Look for Plasmodium parasites.
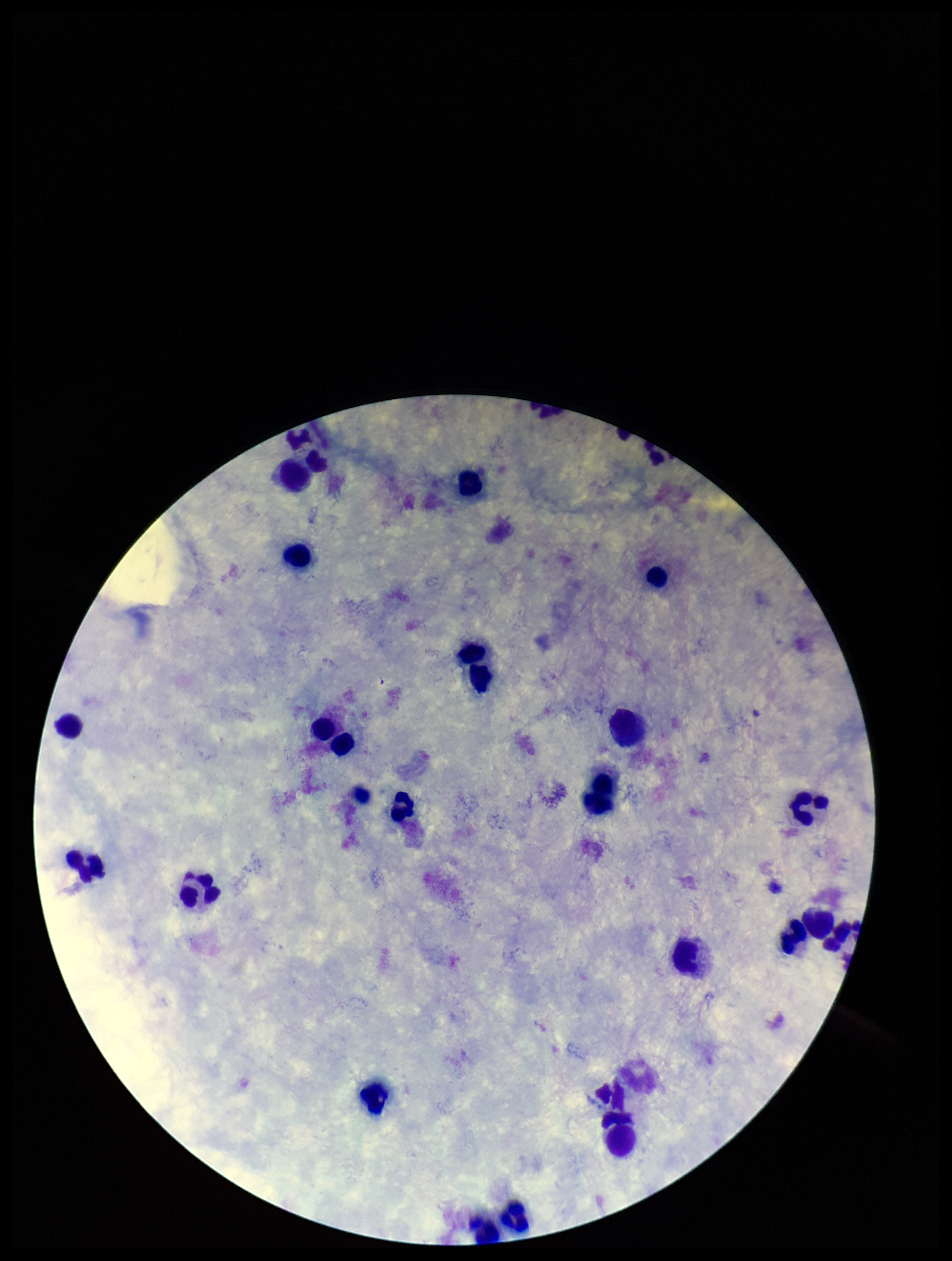
None identified.

Summary:
  - Preparation: thick smear
  - Field of view: single
  - Patient malaria status: negative
  - Parasite count: 0
  - Image size: 952×1261 pixels
  - Leukocyte count: 27
  - Stain: Giemsa
  - Capture: smartphone photograph through the microscope eyepiece